Comment on the morphology of the erythrocytes.
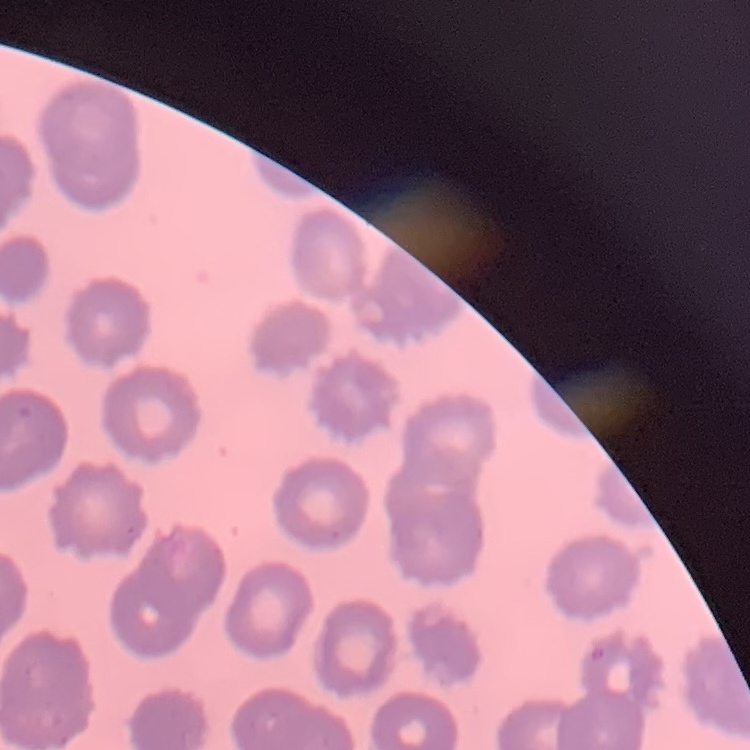
No rouleaux formation.

Thin blood film. Stained with either Field's or Giemsa. Square crop of a larger photomicrograph.